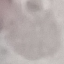
Result: negative for malaria parasites. Photographed with a smartphone camera at the microscope eyepiece. Giemsa-stained preparation. Thin blood smear. Automatically extracted cell patch, resized to 64 × 64 pixels.